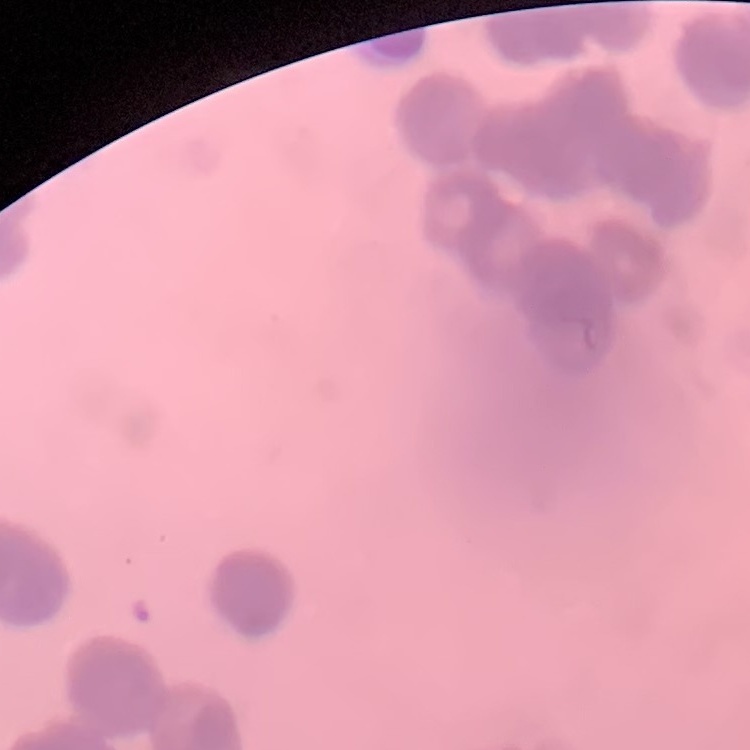
red blood cell morphology = rouleaux formation
preparation = thin blood film
stain = Field's or Giemsa
image type = square crop of a larger photomicrograph